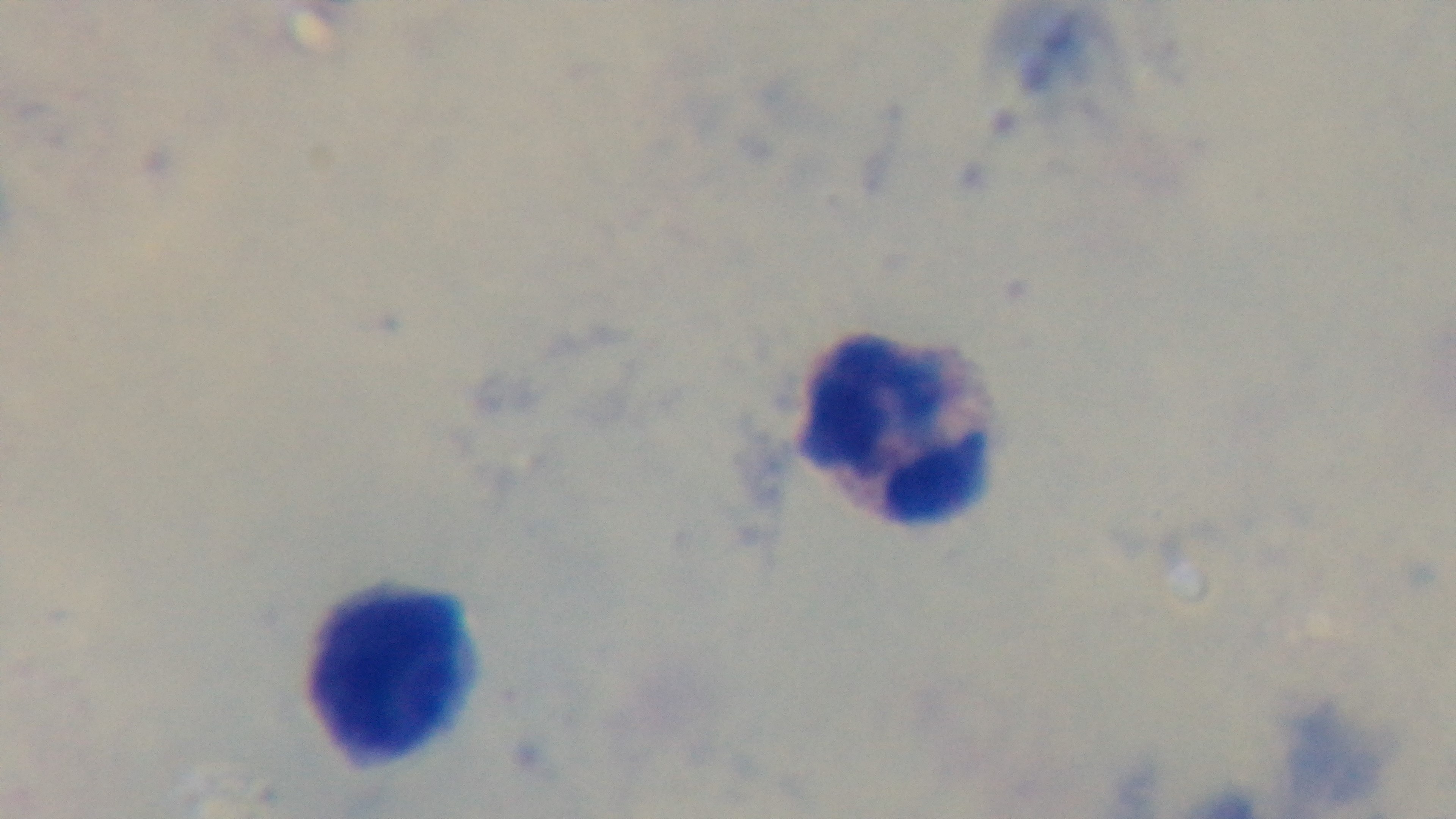

capture = mounted 4K digital camera
preparation = thick blood film
modality = light microscopy
stain = Giemsa
objective = 100x oil immersion
malaria status = uninfected
field of view = one from the slide